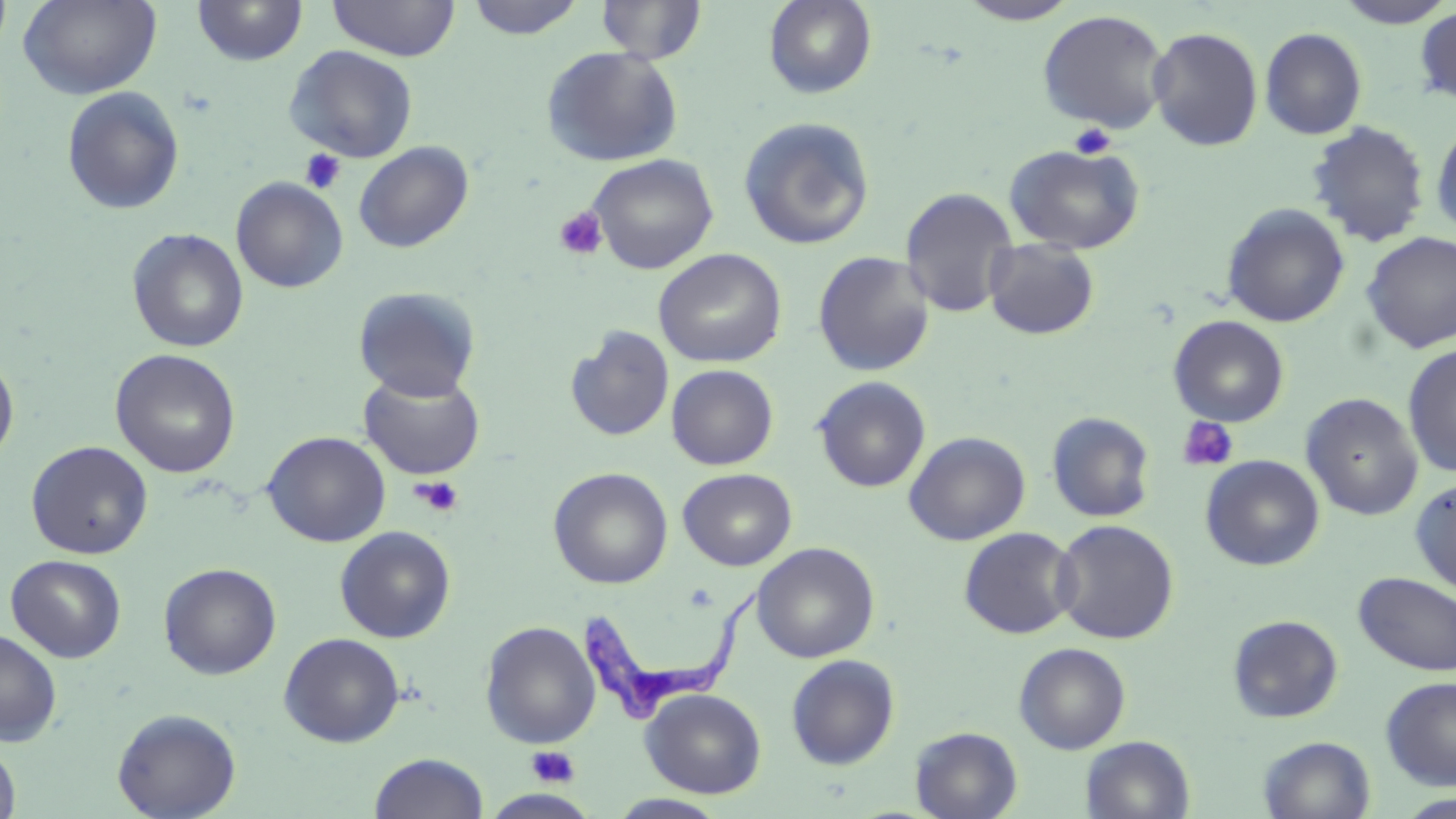

Summary:
  - Coordinate format: approximate bounding boxes as (x1, y1, x2, y2) in pixels
  - Platelet locations: (1068, 122, 1116, 159), (300, 149, 346, 194), (554, 206, 608, 260), (1176, 416, 1239, 472), (410, 476, 464, 517), (526, 745, 581, 788)
  - Trypanosoma brucei locations: (578, 585, 765, 728)
  - Uninfected red blood cell locations: (0, 0, 13, 58), (18, 0, 162, 100), (192, 0, 308, 67), (466, 0, 586, 39), (596, 0, 707, 64), (763, 0, 878, 99), (957, 0, 1081, 25), (1333, 0, 1454, 28), (327, 1, 460, 61), (1414, 6, 1456, 106), (1037, 9, 1172, 134), (1147, 26, 1264, 151), (1260, 27, 1367, 140), (284, 45, 419, 163), (541, 46, 684, 167), (61, 86, 185, 216), (738, 116, 876, 251), (1431, 120, 1456, 238), (1306, 121, 1430, 247), (354, 141, 474, 253), (1003, 143, 1145, 254), (587, 153, 719, 274), (230, 177, 348, 293), (899, 187, 1019, 318), (1221, 203, 1350, 328), (127, 228, 249, 353), (1361, 231, 1456, 353), (983, 239, 1099, 340), (653, 248, 787, 368), (812, 251, 935, 377), (353, 286, 481, 401), (1168, 315, 1290, 426), (565, 325, 674, 442), (1402, 343, 1456, 477), (110, 348, 241, 478), (0, 349, 19, 467), (666, 364, 778, 470), (358, 371, 485, 480), (812, 376, 930, 492), (1300, 393, 1424, 521), (1046, 411, 1156, 523), (262, 431, 391, 547), (903, 431, 1030, 546), (25, 441, 153, 559), (1200, 455, 1325, 571), (549, 467, 673, 589), (678, 468, 796, 570), (1409, 477, 1456, 598), (1051, 519, 1179, 644), (335, 525, 456, 643), (959, 527, 1079, 639), (751, 542, 880, 663), (5, 554, 126, 662), (159, 562, 281, 679), (1353, 571, 1456, 676), (1227, 614, 1344, 723), (479, 620, 601, 749), (0, 629, 62, 746), (279, 632, 405, 747), (1013, 641, 1131, 754), (786, 654, 899, 770), (1380, 676, 1456, 790), (640, 688, 766, 798), (112, 708, 241, 819), (910, 726, 1023, 819), (1081, 736, 1195, 819), (1258, 736, 1376, 819), (0, 741, 21, 819), (369, 752, 489, 819), (1398, 793, 1456, 818), (607, 794, 731, 818)
  - Slide-level diagnosis: Trypanosoma brucei
  - Image size: 1456×819 pixels
  - Modality: light microscopy
  - Stain: May-Grünwald-Giemsa
  - Field of view: one of a larger specimen
  - Magnification: 1000x
  - Preparation: thin blood film